Name the parasite shown.
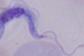
A trypanosome.

Summary:
  - Modality: photomicrograph
  - Magnification: 1000x